Locate the red blood cells and classify each one as Plasmodium falciparum-infected, uninfected, or of indeterminate infection status.
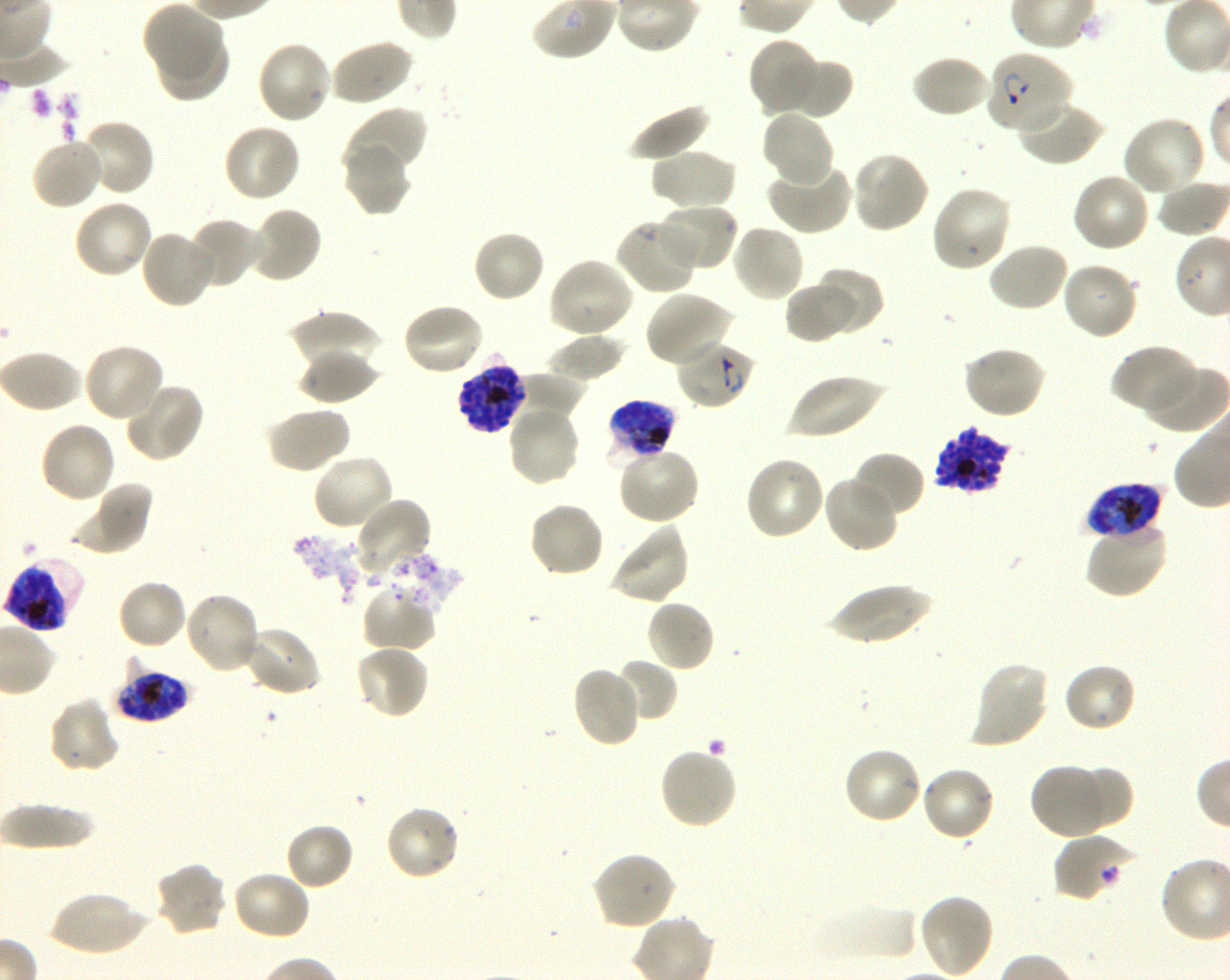
Approximate bounding boxes as {x1, y1, x2, y2} in pixels. Not every red blood cell is marked. A life-cycle stage — or a range of stages, where the recorded stages span more than one — follows each staged infected red blood cell.
Infected red blood cells: {986, 49, 1074, 134} ring; {675, 339, 757, 410} ring; {456, 354, 525, 436} late schizont; {606, 400, 678, 465} late trophozoite to late schizont; {932, 427, 1011, 494} late schizont; {1085, 483, 1162, 541} late trophozoite to late schizont; {2, 558, 83, 634} late trophozoite to late schizont; {114, 661, 191, 722} late trophozoite to late schizont.
Red blood cells of indeterminate infection status: {1053, 833, 1137, 904}.
Uninfected red blood cells: {143, 4, 223, 79}, {156, 34, 230, 102}, {748, 37, 821, 115}, {328, 39, 413, 108}, {255, 40, 332, 126}, {910, 54, 992, 119}, {783, 58, 852, 119}, {1017, 99, 1105, 167}, {627, 102, 712, 163}, {342, 107, 426, 179}, {761, 109, 836, 188}, {1121, 116, 1208, 197}, {77, 119, 155, 197}, {222, 122, 301, 203}, {29, 136, 104, 211}, {343, 142, 413, 217}, {649, 148, 737, 213}, {850, 150, 929, 235}, {765, 160, 854, 236}, {1071, 172, 1152, 254}, {930, 185, 1013, 273}, {72, 199, 154, 279}, {656, 203, 739, 272}, {248, 206, 323, 284}, {190, 217, 264, 289}, {615, 218, 699, 295}, {730, 223, 806, 303}, {139, 228, 219, 309}, {472, 229, 546, 304}, {986, 241, 1070, 313}, {547, 257, 634, 339}, {1060, 261, 1140, 340}, {813, 269, 883, 335}, {784, 280, 855, 344}, {645, 290, 734, 368}, {402, 302, 485, 377}, {290, 311, 380, 376}, {547, 334, 625, 384}, {82, 342, 165, 424}, {1111, 344, 1198, 418}, {960, 346, 1046, 420}, {298, 348, 379, 404}, {0, 349, 84, 414}, {1142, 362, 1226, 434}, {511, 370, 587, 425}, {787, 373, 885, 442}, {122, 381, 204, 462}, {506, 402, 582, 487}, {265, 405, 350, 474}, {38, 420, 117, 504}, {617, 445, 702, 525}, {851, 451, 926, 519}, {311, 453, 396, 532}, {744, 455, 826, 542}, {822, 474, 899, 553}, {70, 483, 152, 557}, {355, 495, 433, 575}, {528, 501, 605, 579}, {1085, 519, 1167, 598}, {608, 523, 691, 605}, {383, 552, 464, 616}, {116, 578, 189, 651}, {826, 583, 933, 646}, {361, 585, 437, 653}, {183, 591, 260, 675}, {644, 598, 716, 673}, {243, 625, 321, 697}, {354, 642, 430, 720}, {614, 659, 678, 723}, {970, 660, 1050, 749}, {1062, 662, 1138, 734}, {571, 666, 642, 748}, {47, 697, 121, 774}, {659, 746, 739, 829}, {841, 746, 925, 825}, {1029, 762, 1110, 840}, {919, 765, 996, 843}, {1074, 765, 1133, 829}, {0, 802, 96, 849}, {384, 805, 462, 883}, {285, 822, 354, 891}, {591, 851, 676, 930}, {153, 861, 228, 938}, {231, 870, 312, 941}, {46, 891, 150, 957}, {917, 894, 995, 979}, {812, 903, 918, 964}.

Blood group of the donor: O+. Life-cycle stages observed: ring, schizont. Thin blood film. Giemsa-stained preparation. Plasmodium falciparum strain 3D7 in shaking in-vitro culture. Image is 1230×980 pixels. 100x objective under oil immersion, numerical aperture 1.30. Single field of view.